Give the extent of all Trypanosoma brucei.
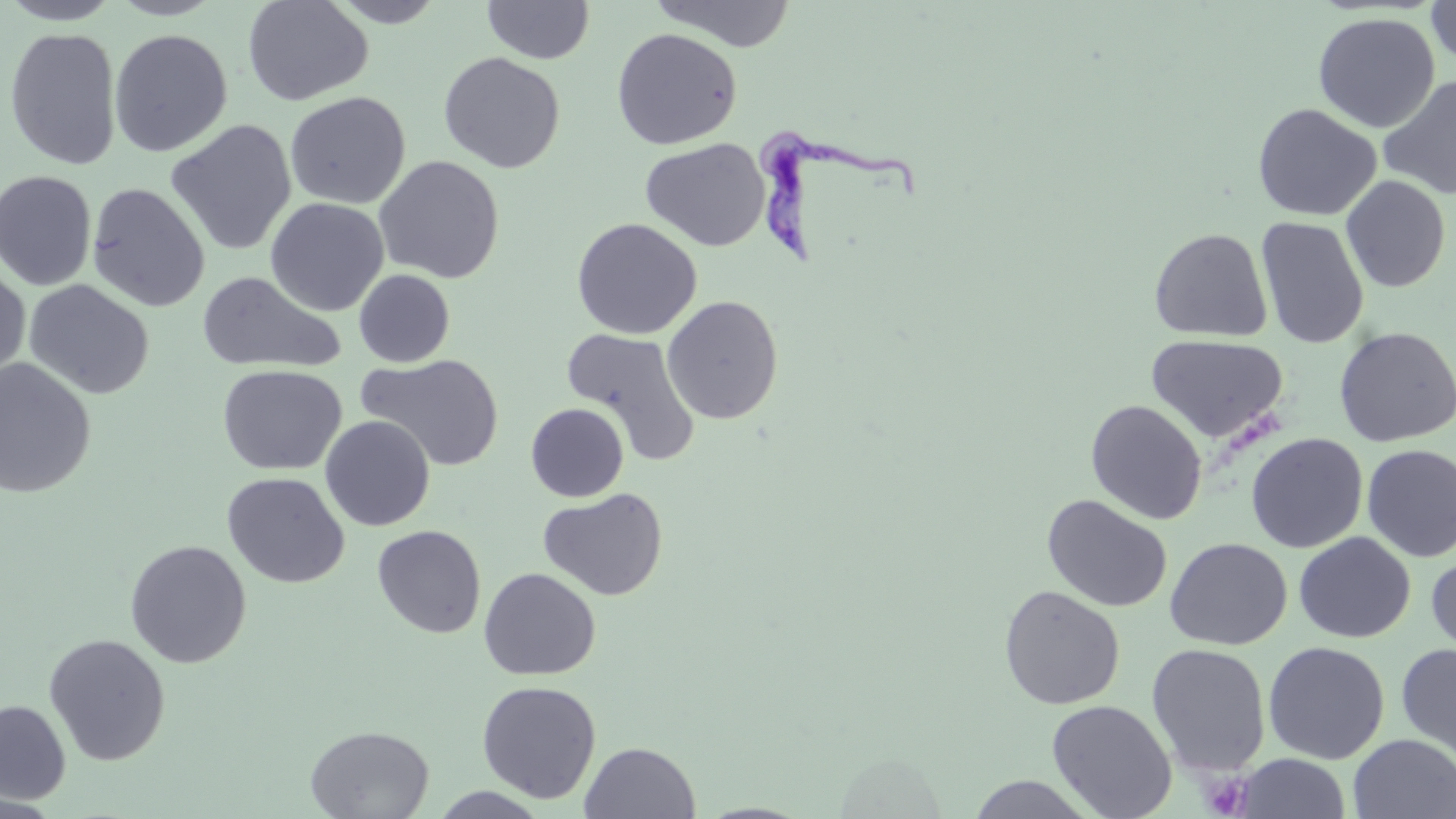
Approximate bounding boxes as named x1/y1/x2/y2 corners in pixels.
Trypanosoma brucei: (x1=750, y1=124, x2=922, y2=267).

slide_level_diagnosis: Trypanosoma brucei
modality: light microscopy
field_of_view: one of a larger specimen
magnification: 1000x
stain: May-Grünwald-Giemsa
image_size: 1456×819 pixels
preparation: thin blood film
uninfected_red_blood_cell_locations: 'approximate bounding boxes as named x1/y1/x2/y2 corners in pixels: (x1=0, y1=0, x2=122, y2=25), (x1=107, y1=0, x2=226, y2=20), (x1=242, y1=0, x2=374, y2=106), (x1=326, y1=0, x2=449, y2=27), (x1=649, y1=0, x2=797, y2=52), (x1=482, y1=1, x2=596, y2=65), (x1=1425, y1=1, x2=1456, y2=70), (x1=1312, y1=12, x2=1440, y2=133), (x1=3, y1=27, x2=123, y2=170), (x1=610, y1=27, x2=743, y2=150), (x1=109, y1=28, x2=233, y2=158), (x1=438, y1=51, x2=566, y2=173), (x1=1378, y1=75, x2=1456, y2=199), (x1=285, y1=91, x2=410, y2=209), (x1=1252, y1=103, x2=1381, y2=221), (x1=165, y1=119, x2=297, y2=256), (x1=639, y1=137, x2=771, y2=251), (x1=374, y1=155, x2=505, y2=284), (x1=0, y1=170, x2=97, y2=290), (x1=1340, y1=175, x2=1451, y2=293), (x1=86, y1=182, x2=210, y2=312), (x1=265, y1=197, x2=389, y2=317), (x1=1256, y1=216, x2=1369, y2=349), (x1=570, y1=217, x2=703, y2=340), (x1=1149, y1=227, x2=1272, y2=342), (x1=0, y1=265, x2=31, y2=383), (x1=353, y1=269, x2=455, y2=367), (x1=196, y1=270, x2=346, y2=375), (x1=23, y1=279, x2=155, y2=399), (x1=662, y1=295, x2=784, y2=425), (x1=1333, y1=325, x2=1456, y2=447), (x1=560, y1=327, x2=702, y2=466), (x1=1146, y1=333, x2=1288, y2=444), (x1=356, y1=353, x2=505, y2=473), (x1=0, y1=358, x2=97, y2=499), (x1=217, y1=364, x2=347, y2=476), (x1=1085, y1=399, x2=1207, y2=524), (x1=526, y1=402, x2=629, y2=502), (x1=319, y1=416, x2=435, y2=531), (x1=1245, y1=432, x2=1368, y2=553), (x1=1361, y1=444, x2=1456, y2=562), (x1=221, y1=472, x2=350, y2=588), (x1=537, y1=488, x2=668, y2=601), (x1=1042, y1=494, x2=1172, y2=612), (x1=372, y1=525, x2=486, y2=638), (x1=1293, y1=531, x2=1416, y2=644), (x1=1164, y1=537, x2=1292, y2=650), (x1=124, y1=540, x2=251, y2=668), (x1=1426, y1=551, x2=1456, y2=663), (x1=478, y1=567, x2=601, y2=680), (x1=999, y1=585, x2=1125, y2=710), (x1=43, y1=633, x2=171, y2=766), (x1=1263, y1=641, x2=1390, y2=764), (x1=1146, y1=643, x2=1272, y2=778), (x1=1396, y1=643, x2=1456, y2=762), (x1=477, y1=680, x2=602, y2=803), (x1=0, y1=699, x2=71, y2=804), (x1=1046, y1=699, x2=1177, y2=819), (x1=305, y1=724, x2=434, y2=818), (x1=1347, y1=735, x2=1456, y2=818), (x1=580, y1=741, x2=701, y2=818), (x1=1233, y1=753, x2=1352, y2=818), (x1=964, y1=774, x2=1098, y2=817), (x1=429, y1=787, x2=551, y2=818), (x1=0, y1=793, x2=63, y2=818)'
platelet_locations: 'approximate bounding boxes as named x1/y1/x2/y2 corners in pixels: (x1=1202, y1=772, x2=1253, y2=817)'